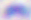 Micrograph. Captured at 400x magnification. Toxoplasma gondii is shown.